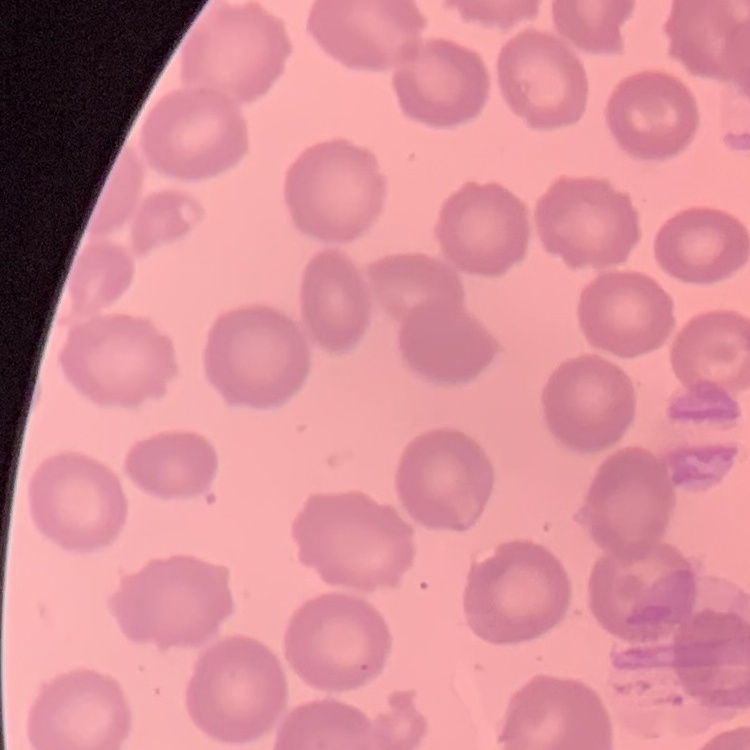

erythrocyte morphology = no rouleaux formation
image type = one tile cut from a larger photomicrograph
preparation = thin peripheral smear
stain = Field's or Giemsa